State which parasite is depicted.
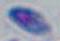
This is Toxoplasma gondii.

magnification = 1000x
modality = micrograph